Comment on the morphology of the red blood cells.
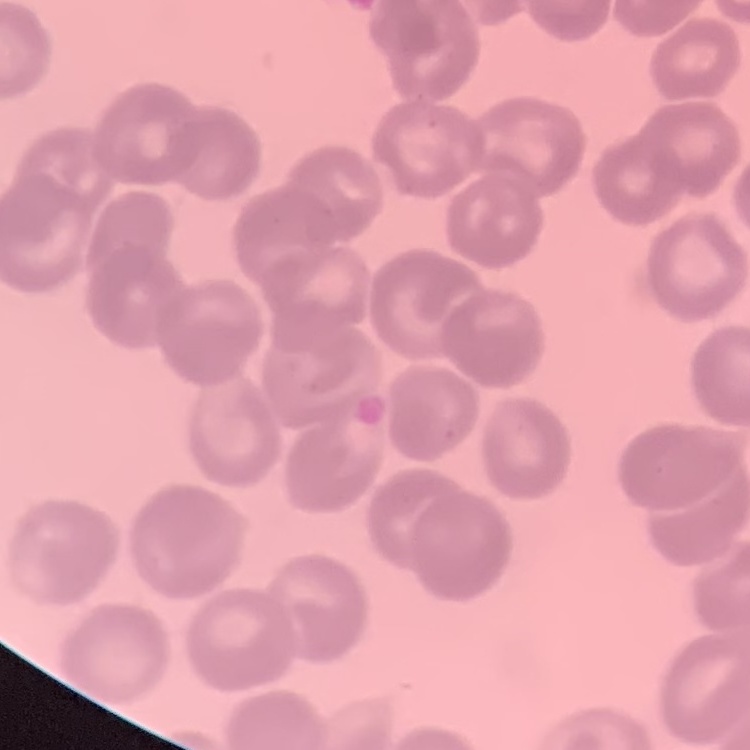

They show rouleaux formation.

preparation = thin peripheral smear
stain = Field's or Giemsa
image type = one tile cut from a larger photomicrograph